Evaluate for Plasmodium parasites.
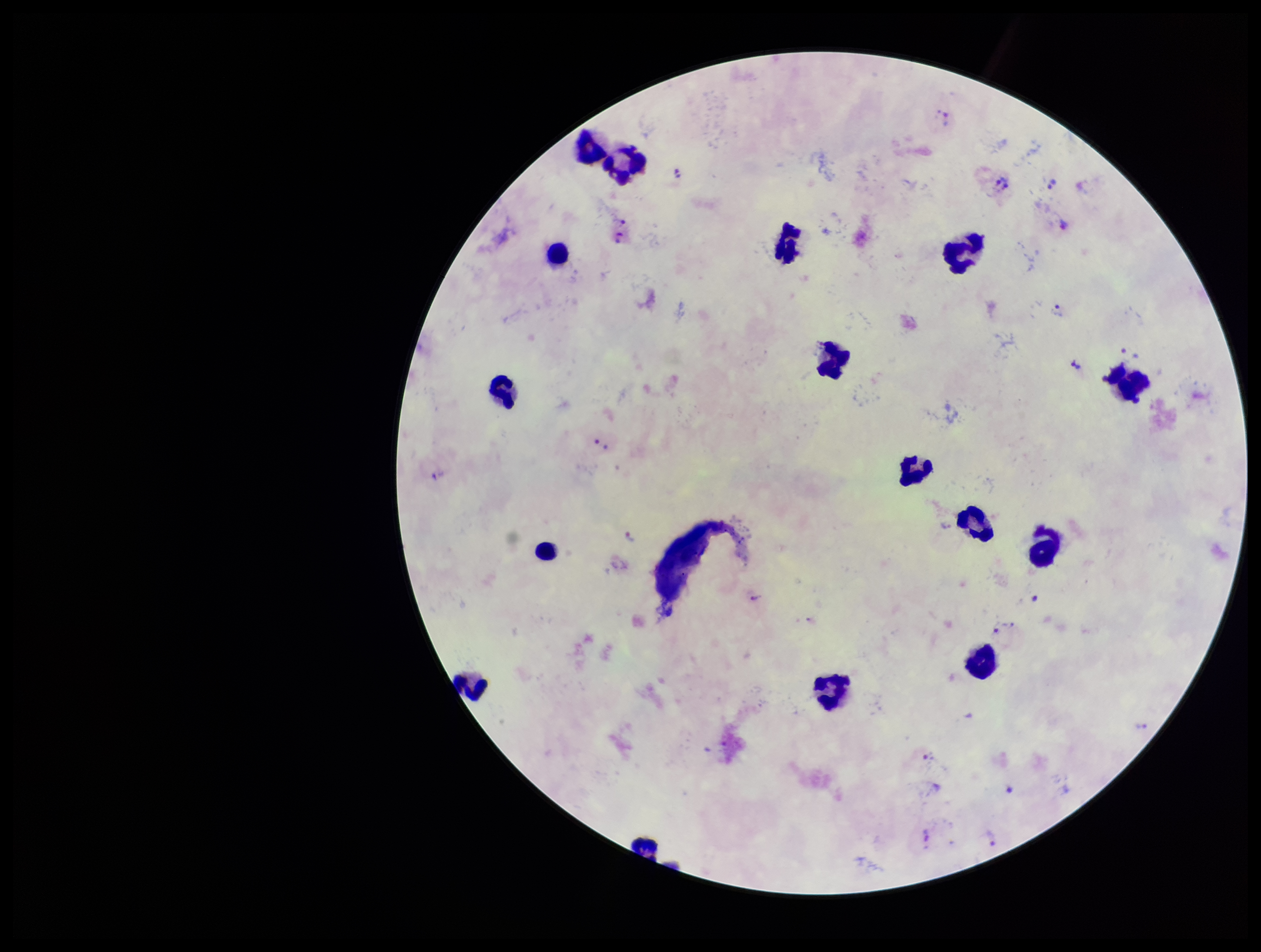
Seen.

Stained with Giemsa. Parasite count: 15. Image is 1261×952 pixels. Preparation: thick smear. Leukocyte count: 16. One field from this slide. Smartphone photograph taken through the eyepiece of a microscope. Species reported for this patient: Plasmodium vivax. Patient malaria status: infected.